Classify this cell by malaria status.
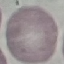
It is uninfected.

Giemsa-stained preparation. Acquired by smartphone through the microscope eyepiece. Cell patch, automatically extracted from a larger field of view and resized to 64 × 64 pixels. Thin blood film.